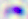

modality: micrograph
identification: Toxoplasma gondii
magnification: 400x